Assess for malaria.
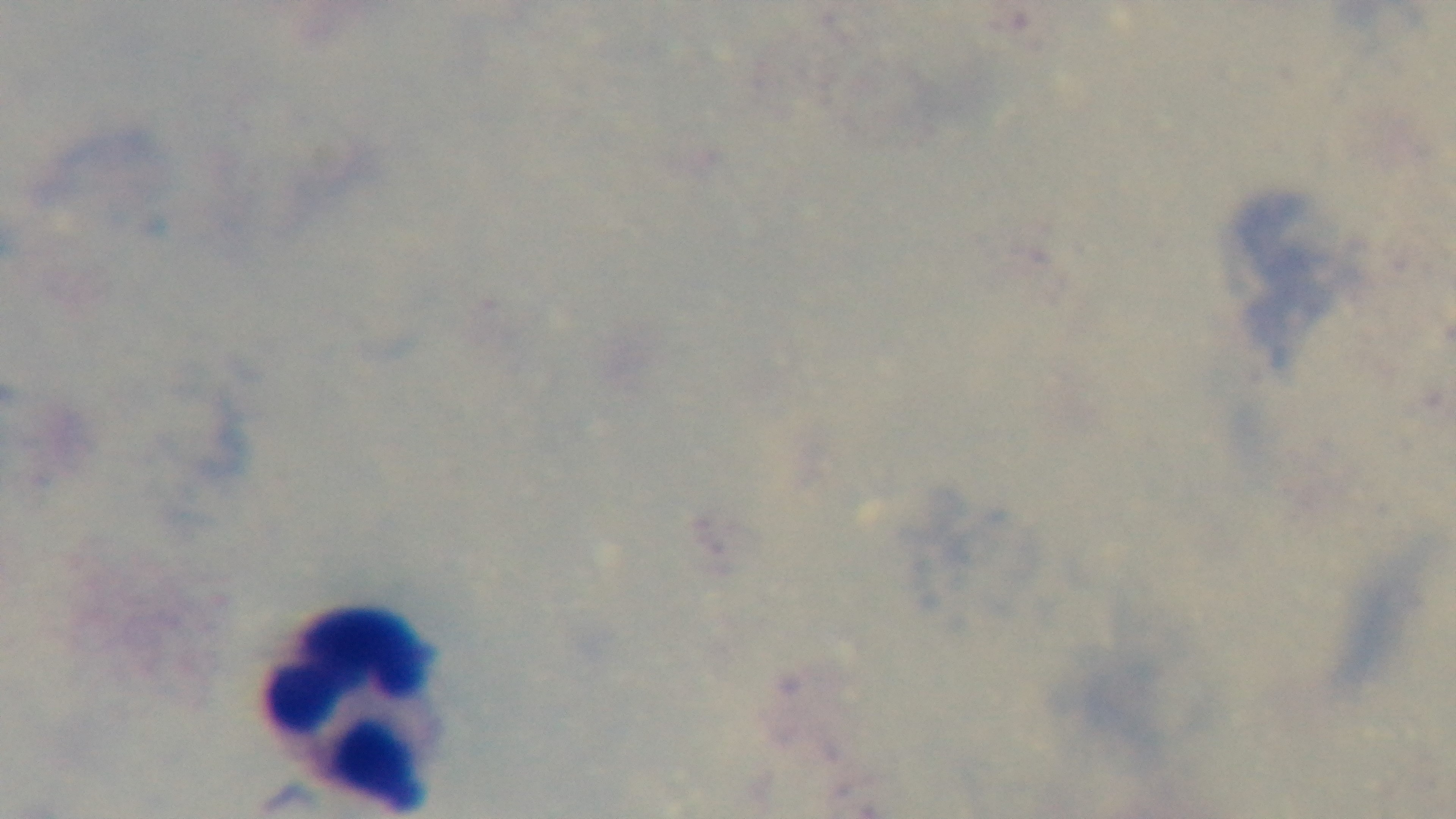
It is uninfected.

Summary:
  - Capture: mounted 4K digital camera
  - Preparation: thick smear
  - Objective: 100x oil immersion
  - Stain: Giemsa
  - Field of view: single
  - Modality: light microscopy